Classify this cell by malaria status.
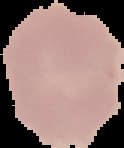
It is uninfected.

Summary:
  - Image size: 124×148 pixels
  - Preparation: thin blood film
  - Image type: segmented cell region with the area outside set to black